State which cell type is depicted.
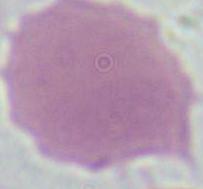
This is an erythrocyte.

magnification = 1000x
modality = micrograph